Assess this cell for malaria.
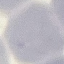
Uninfected.

stain = Giemsa
capture = smartphone camera at the microscope eyepiece
preparation = thin blood film
image type = automatically extracted cell patch, resized to 64 × 64 pixels